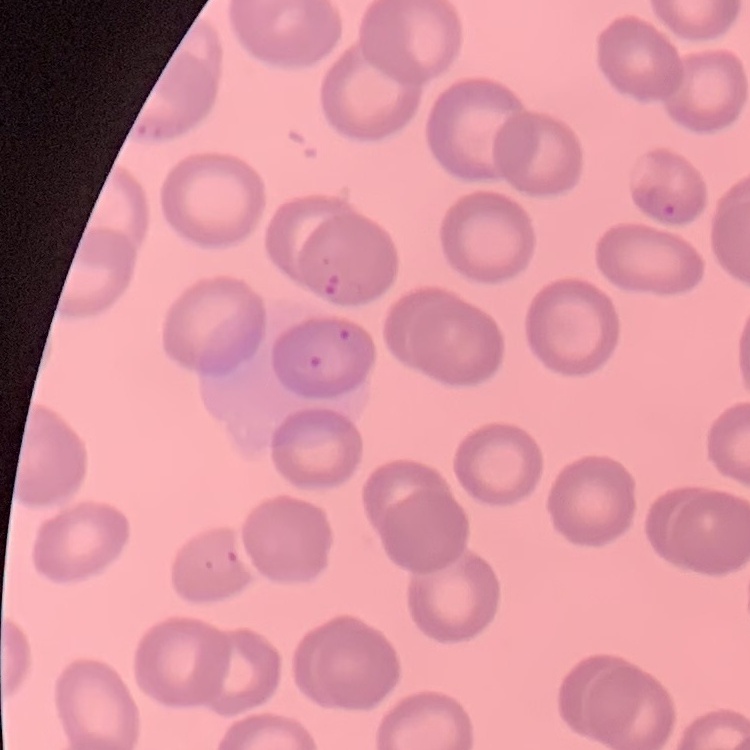

Summary:
  - Red blood cell morphology: no rouleaux formation
  - Preparation: thin peripheral smear
  - Stain: Field's or Giemsa
  - Image type: square crop of a larger photomicrograph